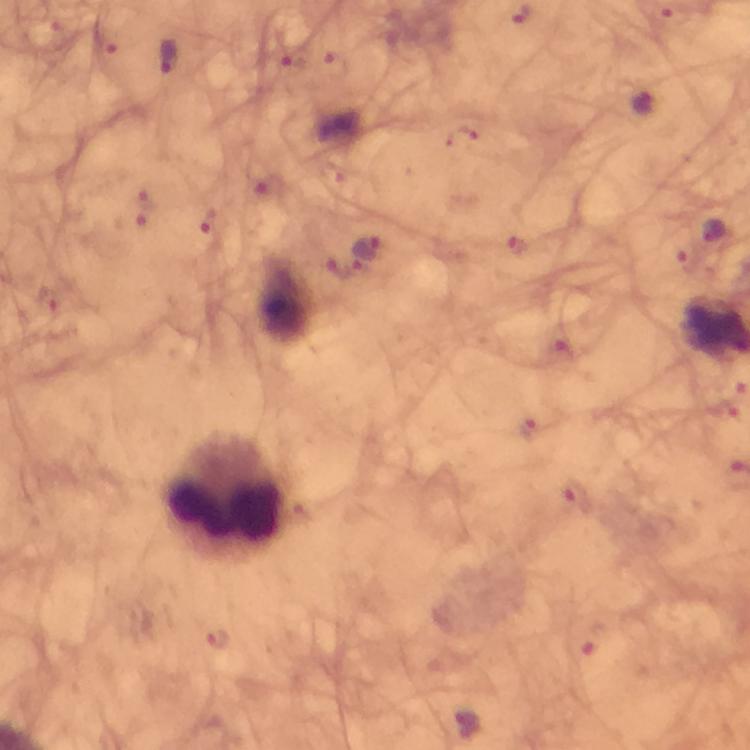

Approximate centers as {x, y} in pixels.
Summary:
  - Leukocyte locations: {226, 495}
  - Malaria parasite locations: {168, 54}, {333, 67}, {644, 104}, {463, 137}, {148, 199}, {210, 221}, {714, 231}, {515, 243}, {368, 249}, {342, 268}, {528, 429}, {578, 495}, {218, 638}, {466, 725}
  - Image size: 750×750 pixels
  - Preparation: thick smear
  - Capture: smartphone photograph through a microscope
  - Context: from a diagnostic examination for malaria
  - Cropped from: one field of view
  - Immersion oil: used
  - Stain: Giemsa
  - Magnification: 100x